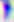

identification = Toxoplasma gondii
modality = photomicrograph
magnification = 400x